Give the preparation type.
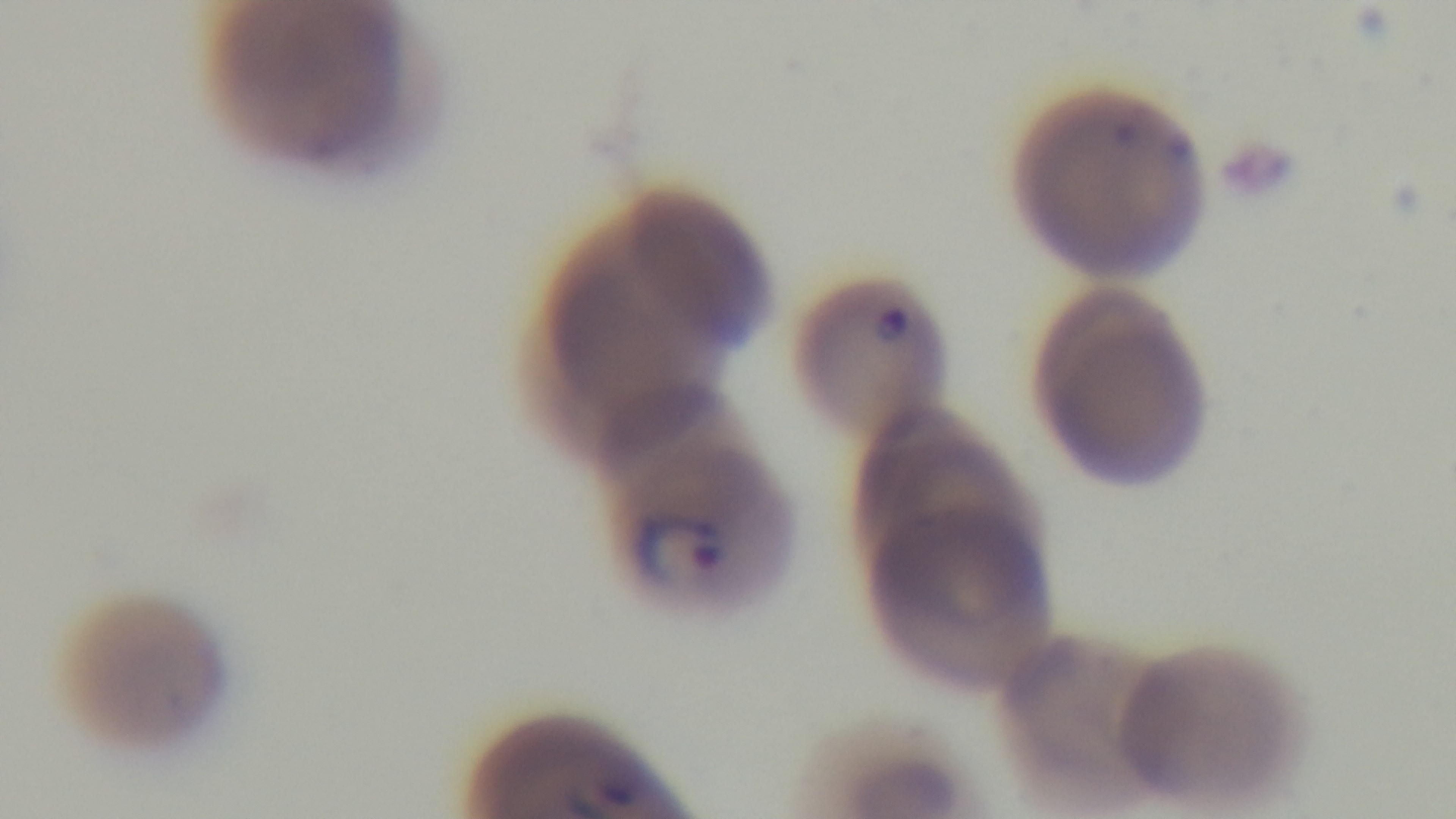
It is a thin blood film.

capture: mounted 4K digital camera
field_of_view: single
stain: Giemsa
malaria_status: positive
modality: light microscopy
objective: 100x oil immersion